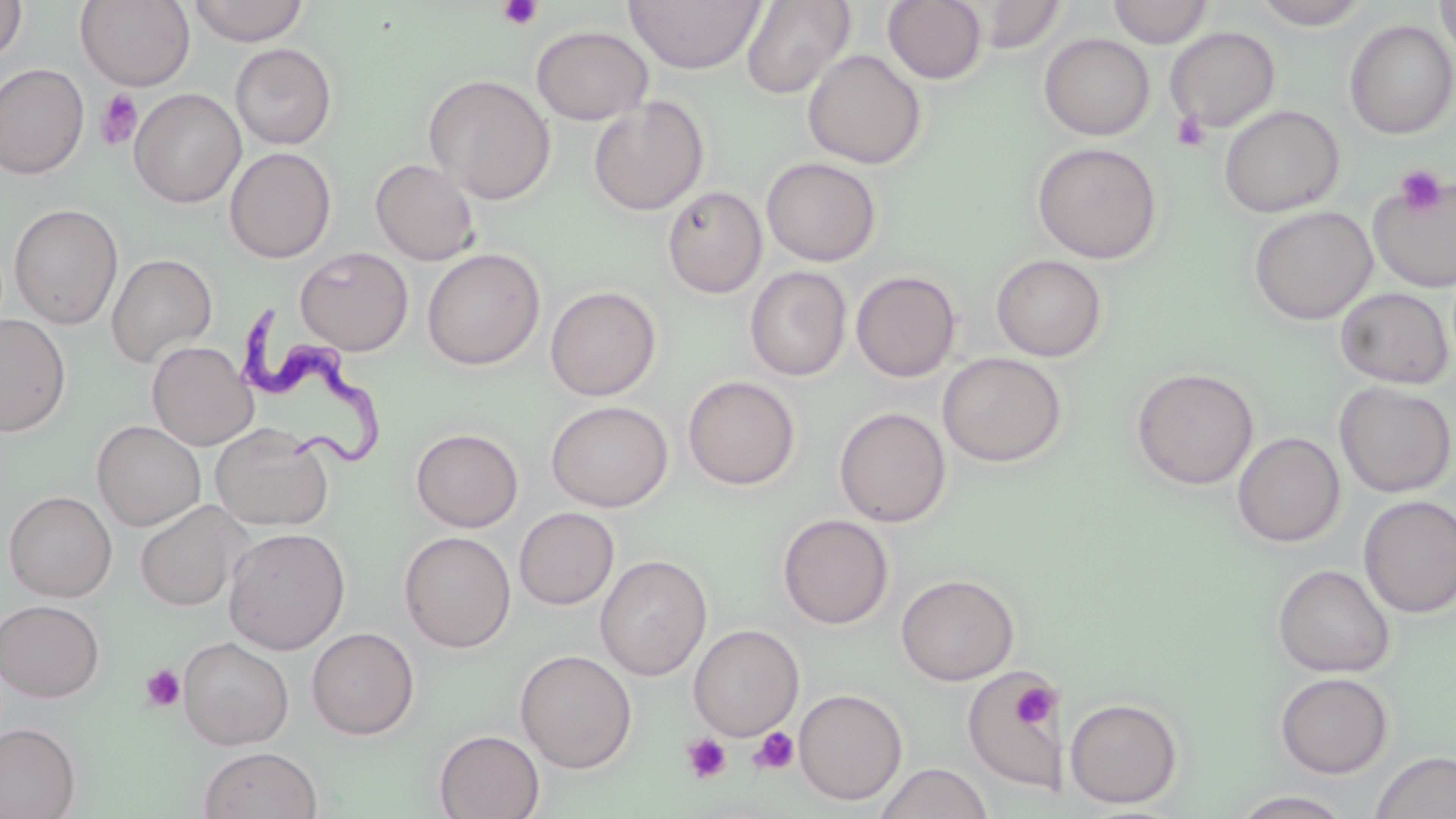

Approximate bounding boxes as [x1, y1, x2, y2] in pixels. Uninfected red blood cell locations: [0, 0, 28, 65], [75, 0, 195, 90], [188, 0, 310, 47], [624, 0, 766, 75], [883, 0, 987, 84], [971, 0, 1068, 53], [1108, 0, 1213, 48], [1251, 0, 1373, 29], [1435, 0, 1456, 67], [740, 1, 856, 99], [1344, 19, 1456, 140], [531, 25, 653, 125], [1165, 26, 1280, 132], [1039, 33, 1155, 141], [229, 43, 338, 150], [803, 49, 926, 170], [0, 63, 89, 179], [423, 73, 557, 205], [129, 88, 247, 208], [588, 96, 710, 216], [1219, 105, 1344, 218], [1031, 141, 1163, 265], [224, 147, 336, 263], [761, 157, 881, 266], [370, 158, 480, 266], [1367, 171, 1456, 293], [662, 186, 767, 298], [8, 203, 124, 329], [1249, 205, 1377, 325], [295, 246, 414, 356], [422, 248, 545, 370], [106, 253, 218, 367], [991, 254, 1108, 362], [745, 267, 851, 381], [851, 270, 961, 382], [545, 285, 662, 401], [1335, 287, 1454, 389], [0, 315, 71, 437], [147, 341, 257, 450], [937, 352, 1067, 467], [1131, 367, 1259, 490], [682, 375, 800, 490], [1334, 381, 1455, 498], [546, 400, 673, 512], [834, 406, 951, 528], [92, 420, 206, 531], [209, 423, 335, 531], [410, 428, 524, 532], [1232, 432, 1345, 547], [4, 490, 117, 602], [1358, 496, 1456, 619], [135, 500, 250, 612], [514, 507, 620, 609], [777, 514, 894, 630], [223, 526, 350, 655], [399, 531, 516, 653], [594, 554, 712, 680], [1272, 563, 1396, 678], [896, 573, 1020, 685], [0, 599, 105, 702], [688, 623, 804, 741], [307, 627, 419, 740], [178, 636, 294, 750], [515, 649, 637, 773], [963, 667, 1059, 793], [1274, 672, 1394, 778], [793, 688, 907, 805], [1064, 697, 1185, 810], [0, 722, 81, 819], [434, 729, 545, 819], [199, 746, 323, 819], [1369, 751, 1456, 819], [874, 763, 994, 819], [1231, 789, 1357, 818]. Trypanosoma brucei locations: [240, 303, 393, 473]. Platelet locations: [497, 0, 544, 31], [95, 89, 143, 150], [1171, 112, 1211, 151], [1394, 164, 1449, 216], [140, 665, 185, 712], [1013, 682, 1055, 729], [748, 727, 799, 775], [681, 732, 732, 784]. Slide-level diagnosis: Trypanosoma brucei. Thin blood smear. 1000x magnification. Optical microscopy. Image is 1456×819 pixels. May-Grünwald-Giemsa stain. One field of a larger specimen.